Assess the morphology of the red blood cells.
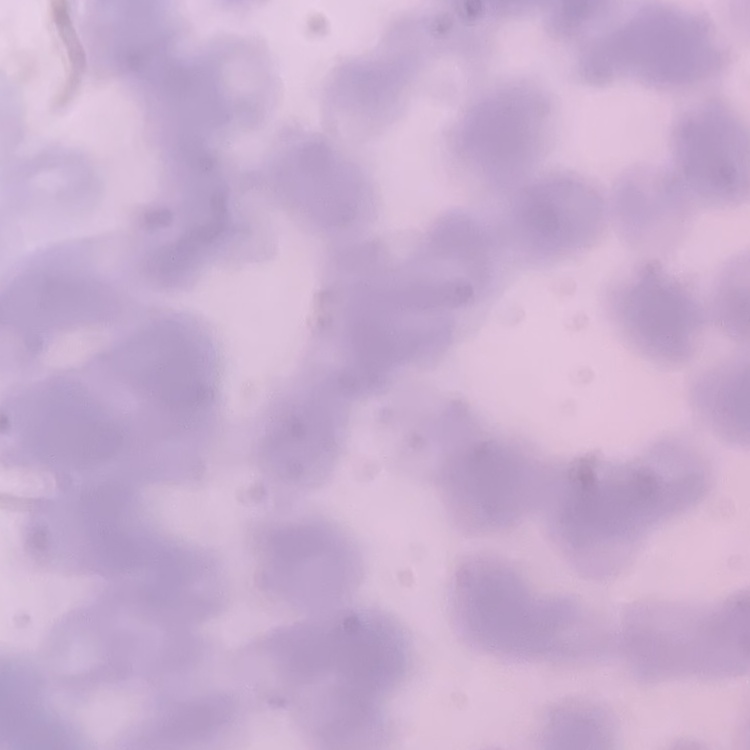

Rouleaux formation.

One tile cut from a larger photomicrograph. Stained with either Field's or Giemsa. Thin peripheral smear.